Report the malaria status of this cell.
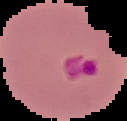
It is parasitized.

The area outside the segmented cell region is set to black. From a thin blood smear. Image is 127×121 pixels.